Report the malaria status of this cell.
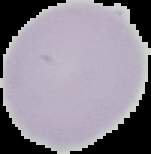
It is uninfected.

image size = 151×154 pixels
image type = segmented cell region with the area outside set to black
preparation = thin blood film